Identify the parasite.
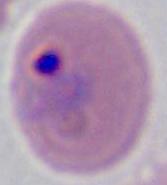
Plasmodium.

Summary:
  - Magnification: 400x or 1000x
  - Modality: micrograph